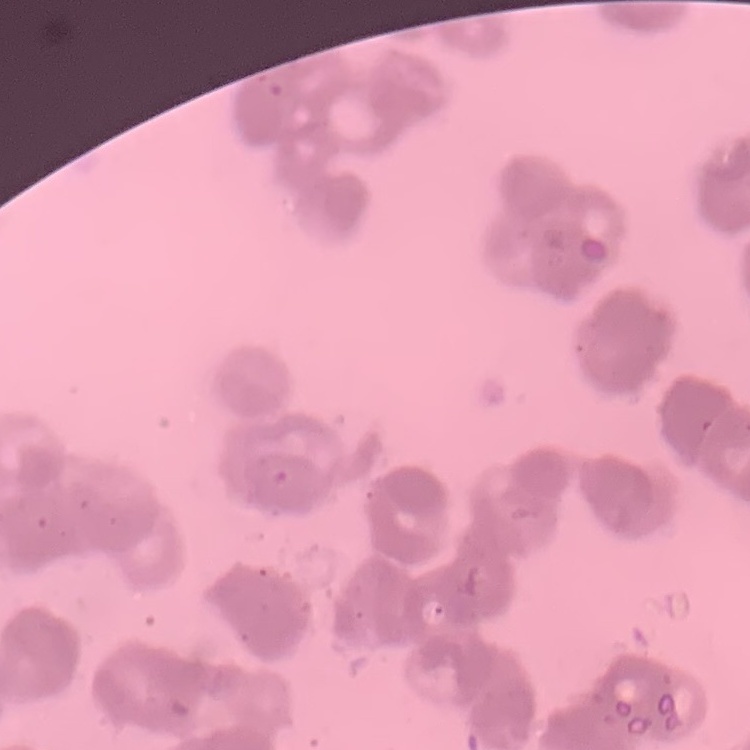

erythrocyte_morphology: rouleaux formation
preparation: thin peripheral smear
image_type: square crop of a larger photomicrograph
stain: Field's or Giemsa